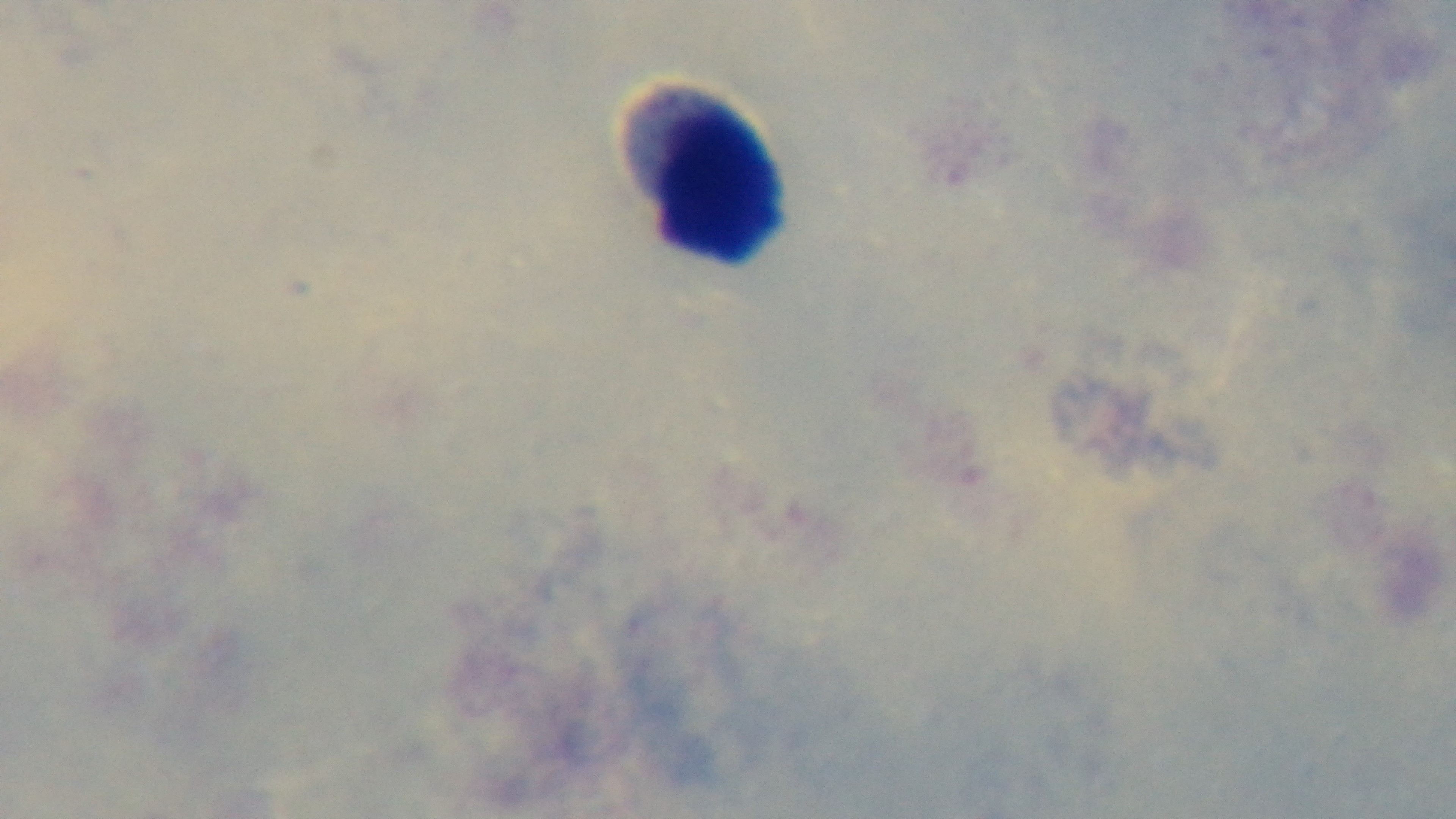

Summary:
  - Field of view: single
  - Objective: 100x oil immersion
  - Capture: mounted 4K digital camera
  - Modality: light microscopy
  - Stain: Giemsa
  - Malaria status: uninfected
  - Preparation: thick smear